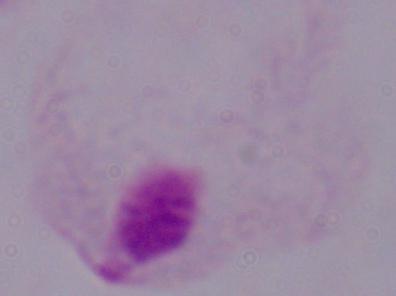

magnification: 1000x
modality: photomicrograph
identification: trichomonad